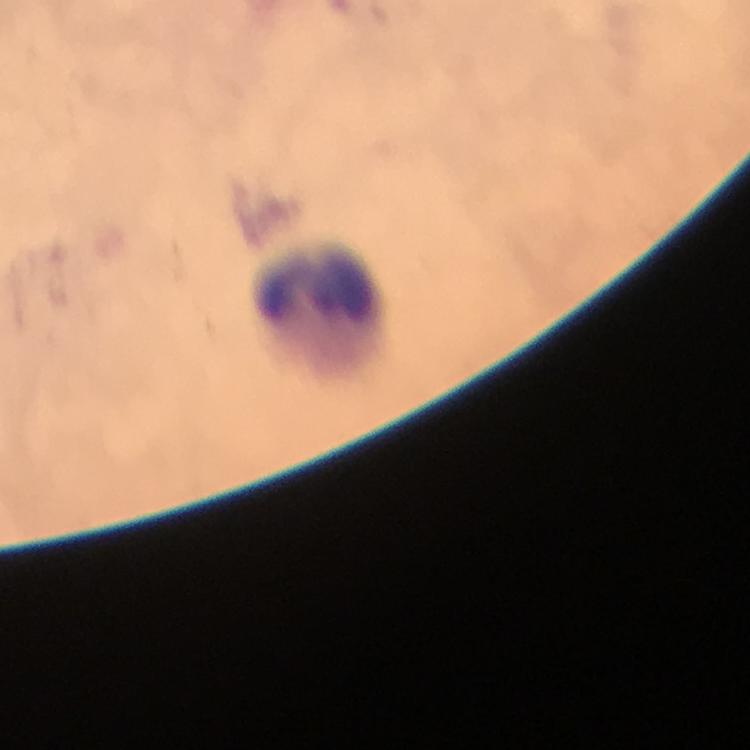

Approximate object centers, in pixels from the top-left corner.
Summary:
  - Leukocyte locations: (x=318, y=300)
  - Immersion oil: used
  - Malaria parasites: none seen
  - Image size: 750×750 pixels
  - Stain: Giemsa
  - Preparation: thick smear
  - Magnification: 100x
  - Cropped from: a single field of view
  - Capture: smartphone mounted on the microscope
  - Context: from a malaria diagnostic workup